Comment on the morphology of the erythrocytes.
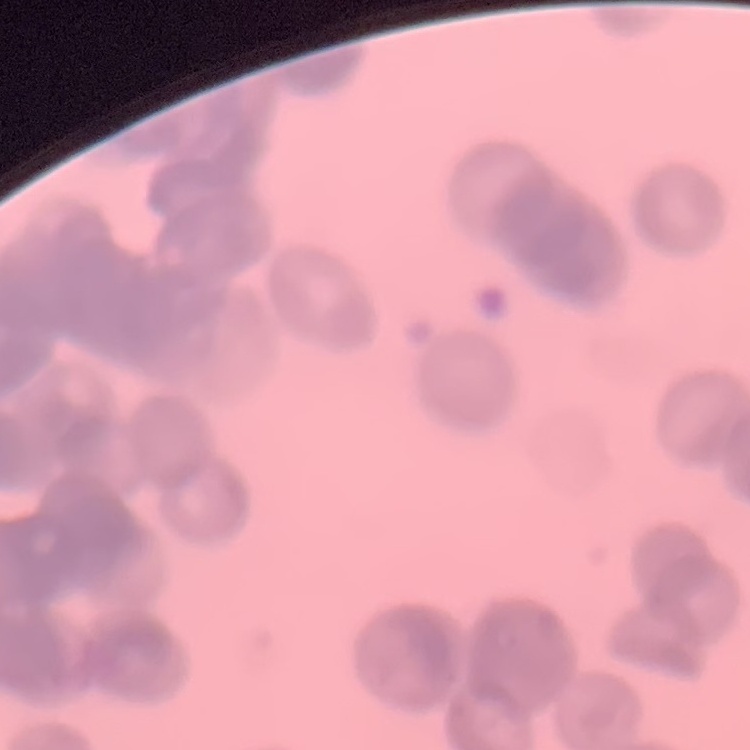
They show rouleaux formation.

Summary:
  - Preparation: thin blood film
  - Stain: Field's or Giemsa
  - Image type: one tile cut from a larger photomicrograph